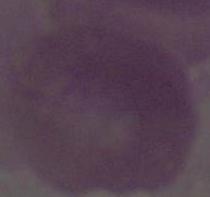
Summary:
  - Modality: micrograph
  - Identification: erythrocyte
  - Magnification: 1000x